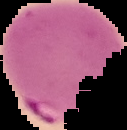
Summary:
  - Image type: segmented cell region with the area outside set to black
  - Preparation: thin blood smear
  - Image size: 127×130 pixels
  - Result: malaria parasites detected